Assess the morphology of the erythrocytes.
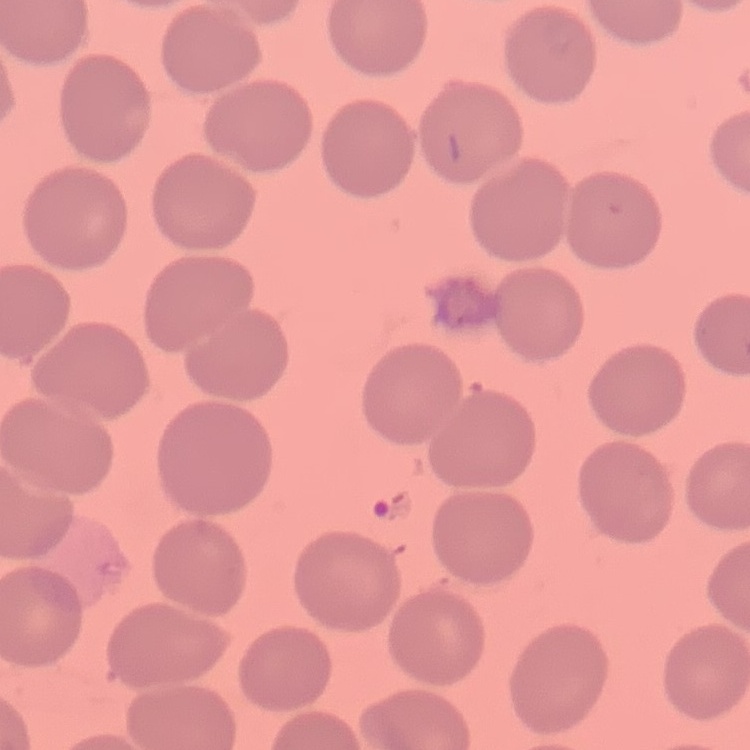
They show no rouleaux formation.

image type = square crop of a larger photomicrograph
preparation = thin blood smear
stain = Field's or Giemsa